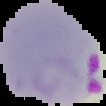
Image is 106×106 pixels. Malaria status: parasitized. From a thin blood smear. Cell region segmented out of the field of view; the surrounding area is masked to black.